Report the malaria status of this cell.
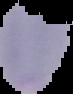
Uninfected.

Summary:
  - Image size: 73×94 pixels
  - Preparation: thin blood smear
  - Image type: segmented cell region with the area outside set to black